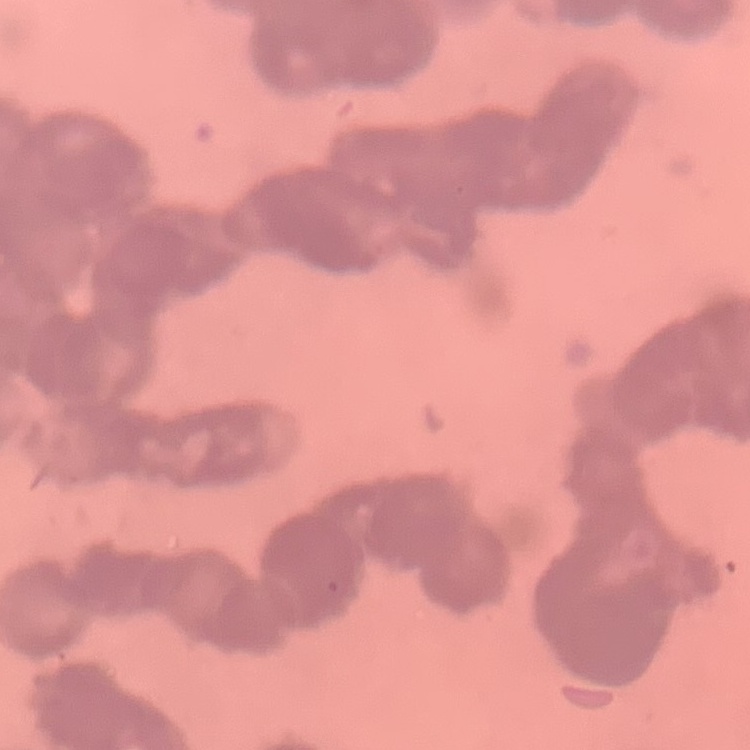
The red blood cells show rouleaux formation. Field's or Giemsa stain. One tile cut from a larger photomicrograph. Thin blood film.